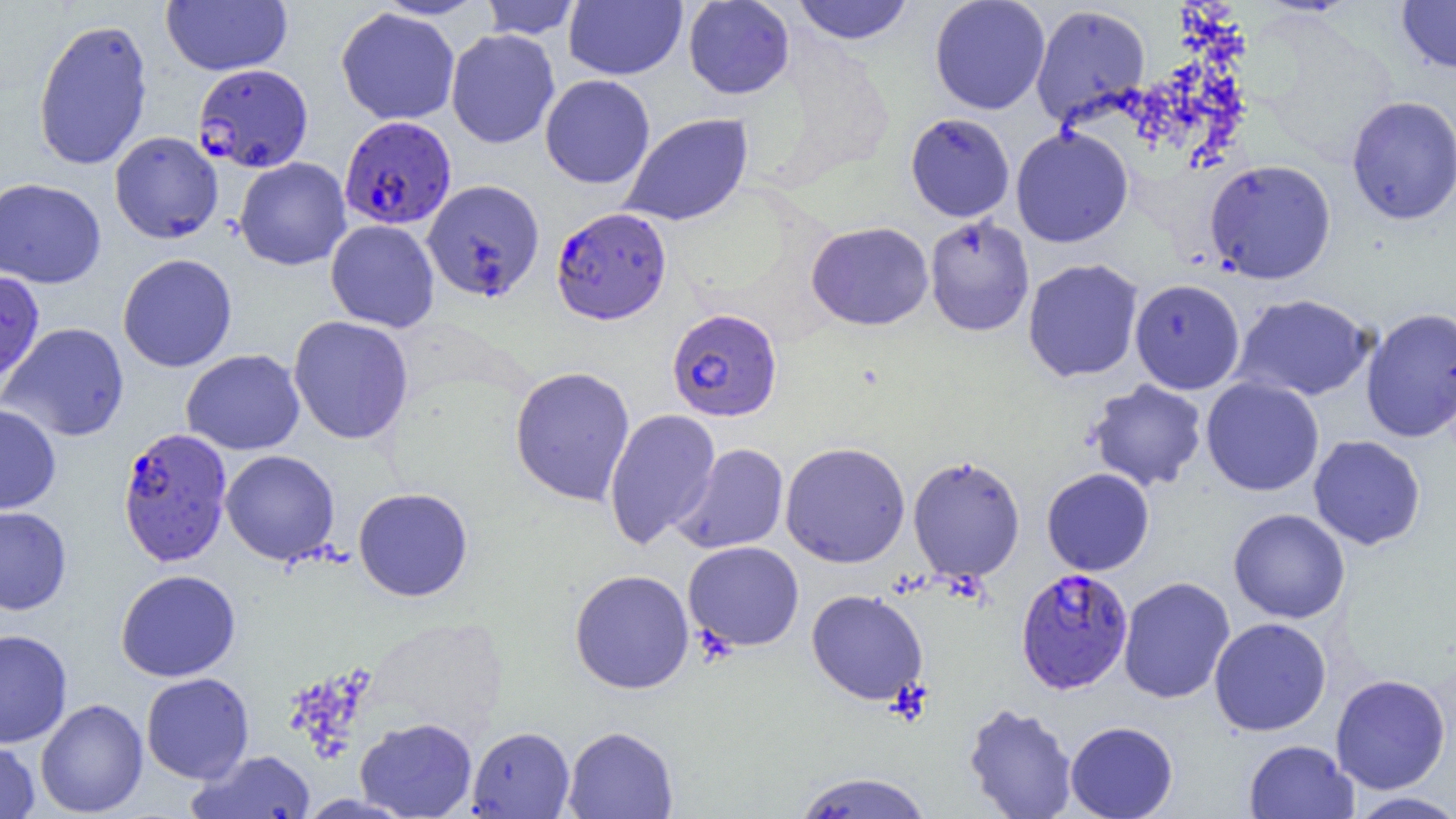

Approximate bounding boxes as (x1,y1)-(x2,y2) corner pairs in pixels. Plasmodium falciparum-infected red blood cell locations: (194,63)-(313,173), (339,115)-(456,230), (551,207)-(671,325), (667,308)-(782,422), (117,427)-(233,567), (1015,567)-(1134,693). Uninfected red blood cell locations: (478,0)-(582,40), (564,0)-(687,80), (792,0)-(914,45), (929,0)-(1051,115), (1396,0)-(1456,75), (161,1)-(292,75), (683,1)-(795,99), (1030,4)-(1151,129), (336,7)-(460,125), (32,17)-(154,172), (446,29)-(559,149), (540,74)-(655,189), (1346,95)-(1456,225), (620,113)-(754,227), (905,113)-(1015,222), (1011,126)-(1133,247), (109,131)-(224,244), (234,157)-(351,270), (1205,159)-(1337,284), (0,177)-(106,289), (421,179)-(545,301), (924,215)-(1035,337), (325,219)-(440,333), (806,221)-(934,331), (117,254)-(237,372), (1022,258)-(1144,382), (0,270)-(45,389), (1130,278)-(1245,394), (1232,294)-(1375,402), (1360,307)-(1456,443), (288,315)-(414,444), (0,322)-(130,443), (180,349)-(305,455), (509,366)-(635,506), (1200,377)-(1325,497), (1085,379)-(1208,492), (0,404)-(61,514), (604,408)-(721,550), (1308,435)-(1426,550), (780,441)-(911,568), (671,443)-(789,554), (220,449)-(340,565), (908,455)-(1025,582), (1041,468)-(1154,576), (352,487)-(473,601), (0,506)-(72,615), (1228,508)-(1351,624), (683,541)-(804,651), (569,568)-(695,694), (115,569)-(241,682), (1118,576)-(1235,704), (806,589)-(928,705), (1208,617)-(1332,736), (0,628)-(73,749), (140,672)-(254,783), (1330,673)-(1452,795), (35,698)-(149,817), (963,702)-(1078,819), (355,717)-(478,818), (1065,721)-(1178,819), (563,725)-(679,818), (467,726)-(575,818), (0,739)-(40,818), (1243,740)-(1358,819), (187,750)-(316,818), (792,771)-(933,818), (1346,791)-(1456,819). Slide-level diagnosis: Plasmodium falciparum. Thin blood smear. Single field of view. Light microscopy. Captured at 1000x magnification. Image is 1456×819 pixels.